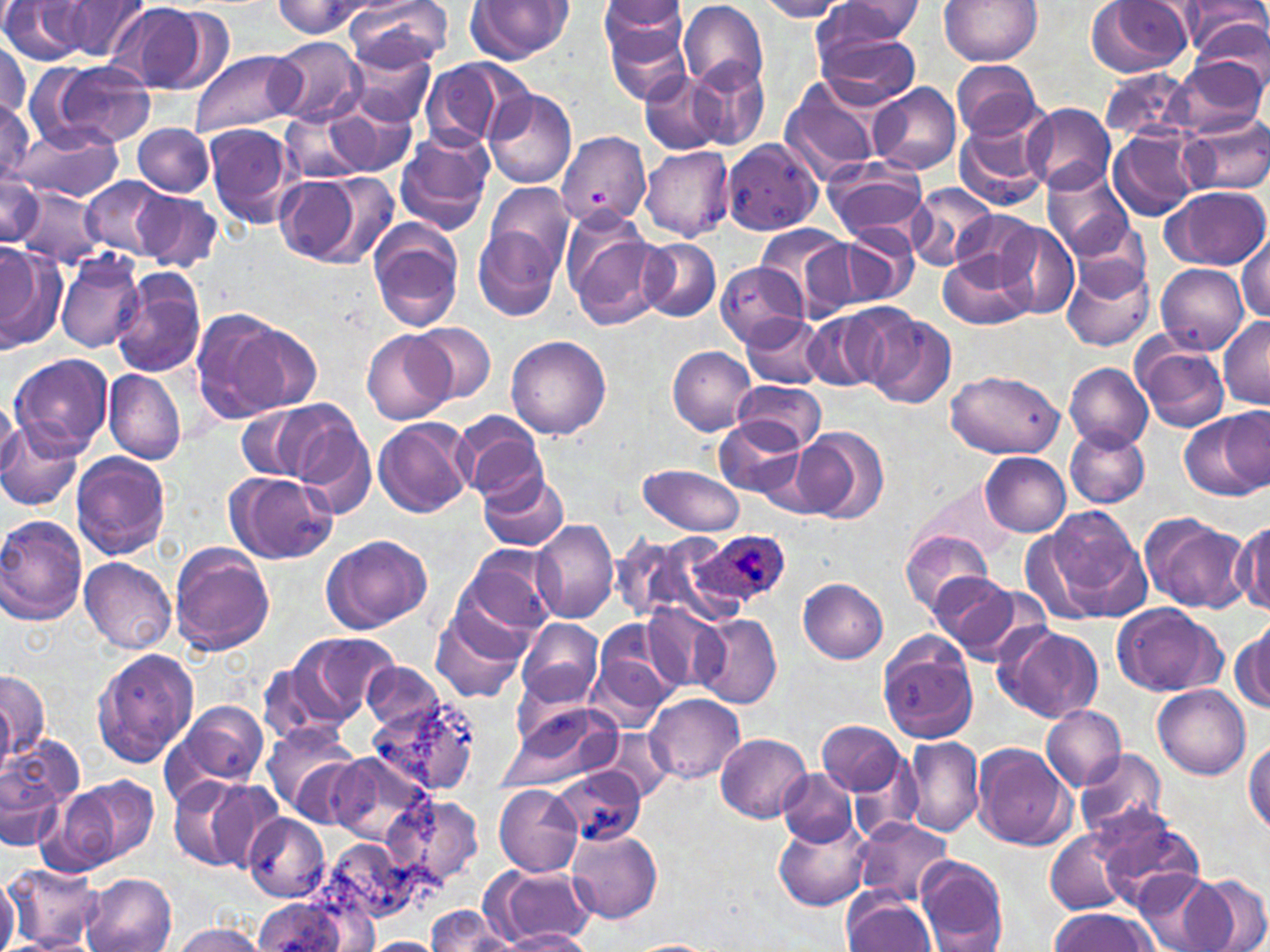

slide_level_diagnosis: Plasmodium ovale
uninfected_red_blood_cell_locations: 'approximate bounding boxes as named x1/y1/x2/y2 corners in pixels: (x1=1, y1=0, x2=90, y2=63), (x1=60, y1=0, x2=151, y2=62), (x1=275, y1=0, x2=376, y2=36), (x1=345, y1=0, x2=451, y2=73), (x1=464, y1=0, x2=573, y2=65), (x1=597, y1=0, x2=691, y2=86), (x1=756, y1=0, x2=848, y2=21), (x1=939, y1=0, x2=1042, y2=66), (x1=1085, y1=0, x2=1194, y2=78), (x1=1177, y1=0, x2=1268, y2=58), (x1=817, y1=1, x2=924, y2=53), (x1=679, y1=2, x2=768, y2=95), (x1=105, y1=3, x2=216, y2=95), (x1=126, y1=12, x2=264, y2=116), (x1=1190, y1=17, x2=1269, y2=88), (x1=814, y1=29, x2=922, y2=110), (x1=268, y1=37, x2=366, y2=126), (x1=0, y1=40, x2=30, y2=121), (x1=346, y1=46, x2=437, y2=128), (x1=189, y1=50, x2=301, y2=138), (x1=1171, y1=55, x2=1267, y2=137), (x1=688, y1=57, x2=770, y2=150), (x1=31, y1=59, x2=158, y2=151), (x1=950, y1=59, x2=1040, y2=141), (x1=418, y1=60, x2=512, y2=150), (x1=639, y1=68, x2=729, y2=155), (x1=1103, y1=70, x2=1196, y2=143), (x1=780, y1=77, x2=888, y2=182), (x1=868, y1=81, x2=962, y2=174), (x1=483, y1=87, x2=576, y2=189), (x1=0, y1=95, x2=48, y2=185), (x1=325, y1=104, x2=415, y2=177), (x1=1024, y1=104, x2=1114, y2=195), (x1=284, y1=109, x2=372, y2=185), (x1=954, y1=114, x2=1053, y2=212), (x1=1182, y1=116, x2=1270, y2=195), (x1=203, y1=122, x2=304, y2=230), (x1=132, y1=124, x2=215, y2=196), (x1=13, y1=127, x2=124, y2=201), (x1=394, y1=129, x2=495, y2=234), (x1=556, y1=131, x2=650, y2=230), (x1=1110, y1=131, x2=1199, y2=221), (x1=720, y1=138, x2=826, y2=239), (x1=640, y1=144, x2=735, y2=240), (x1=823, y1=159, x2=929, y2=246), (x1=1044, y1=166, x2=1135, y2=258), (x1=305, y1=170, x2=401, y2=267), (x1=0, y1=173, x2=42, y2=245), (x1=270, y1=174, x2=364, y2=265), (x1=81, y1=176, x2=173, y2=260), (x1=485, y1=184, x2=574, y2=274), (x1=905, y1=184, x2=1000, y2=270), (x1=18, y1=186, x2=104, y2=269), (x1=1164, y1=186, x2=1268, y2=270), (x1=134, y1=189, x2=223, y2=273), (x1=948, y1=208, x2=1044, y2=291), (x1=565, y1=219, x2=668, y2=330), (x1=367, y1=220, x2=466, y2=332), (x1=994, y1=220, x2=1081, y2=318), (x1=753, y1=223, x2=853, y2=316), (x1=840, y1=223, x2=917, y2=305), (x1=473, y1=227, x2=563, y2=321), (x1=1238, y1=233, x2=1269, y2=322), (x1=637, y1=238, x2=722, y2=322), (x1=0, y1=240, x2=64, y2=354), (x1=939, y1=248, x2=1035, y2=330), (x1=55, y1=250, x2=145, y2=354), (x1=1061, y1=255, x2=1153, y2=353), (x1=718, y1=262, x2=805, y2=346), (x1=1155, y1=263, x2=1248, y2=354), (x1=111, y1=271, x2=207, y2=378), (x1=188, y1=306, x2=310, y2=426), (x1=802, y1=310, x2=896, y2=391), (x1=861, y1=310, x2=957, y2=409), (x1=741, y1=313, x2=831, y2=388), (x1=1218, y1=314, x2=1270, y2=406), (x1=408, y1=321, x2=496, y2=406), (x1=362, y1=330, x2=453, y2=424), (x1=505, y1=335, x2=613, y2=438), (x1=1132, y1=338, x2=1229, y2=433), (x1=667, y1=345, x2=757, y2=434), (x1=8, y1=353, x2=114, y2=457), (x1=1064, y1=362, x2=1153, y2=453), (x1=104, y1=368, x2=186, y2=465), (x1=945, y1=370, x2=1064, y2=458), (x1=733, y1=378, x2=826, y2=452), (x1=0, y1=397, x2=22, y2=477), (x1=282, y1=404, x2=376, y2=518), (x1=235, y1=406, x2=325, y2=483), (x1=453, y1=411, x2=547, y2=501), (x1=1178, y1=411, x2=1269, y2=500), (x1=373, y1=418, x2=472, y2=519), (x1=715, y1=418, x2=807, y2=500), (x1=0, y1=419, x2=86, y2=514), (x1=793, y1=427, x2=889, y2=524), (x1=1065, y1=428, x2=1148, y2=508), (x1=70, y1=452, x2=171, y2=560), (x1=981, y1=454, x2=1070, y2=537), (x1=638, y1=463, x2=746, y2=537), (x1=224, y1=471, x2=339, y2=564), (x1=479, y1=471, x2=570, y2=551), (x1=915, y1=477, x2=1018, y2=564), (x1=1036, y1=504, x2=1150, y2=620), (x1=1140, y1=513, x2=1250, y2=610), (x1=0, y1=515, x2=89, y2=625), (x1=531, y1=519, x2=619, y2=625), (x1=1232, y1=521, x2=1268, y2=613), (x1=900, y1=529, x2=996, y2=616), (x1=612, y1=530, x2=734, y2=629), (x1=320, y1=534, x2=433, y2=634), (x1=461, y1=542, x2=560, y2=637), (x1=168, y1=543, x2=275, y2=655), (x1=437, y1=547, x2=545, y2=691), (x1=79, y1=557, x2=178, y2=653), (x1=930, y1=569, x2=1028, y2=658), (x1=799, y1=579, x2=888, y2=663), (x1=1111, y1=602, x2=1226, y2=697), (x1=643, y1=603, x2=729, y2=693), (x1=431, y1=609, x2=530, y2=704), (x1=696, y1=613, x2=781, y2=708), (x1=517, y1=619, x2=604, y2=705), (x1=1233, y1=621, x2=1270, y2=714), (x1=996, y1=624, x2=1102, y2=725), (x1=589, y1=627, x2=681, y2=728), (x1=283, y1=630, x2=399, y2=729), (x1=877, y1=630, x2=980, y2=743), (x1=92, y1=647, x2=199, y2=768), (x1=363, y1=662, x2=445, y2=732), (x1=0, y1=669, x2=49, y2=767), (x1=1153, y1=684, x2=1250, y2=779), (x1=645, y1=694, x2=744, y2=785), (x1=370, y1=695, x2=481, y2=799), (x1=173, y1=699, x2=268, y2=791), (x1=499, y1=702, x2=623, y2=794), (x1=1041, y1=705, x2=1125, y2=790), (x1=260, y1=721, x2=361, y2=822), (x1=817, y1=721, x2=908, y2=797), (x1=0, y1=732, x2=85, y2=844), (x1=715, y1=732, x2=812, y2=823), (x1=901, y1=735, x2=984, y2=836), (x1=1246, y1=736, x2=1270, y2=834), (x1=971, y1=742, x2=1075, y2=850), (x1=1074, y1=748, x2=1167, y2=843), (x1=321, y1=752, x2=432, y2=848), (x1=553, y1=766, x2=645, y2=846), (x1=778, y1=768, x2=858, y2=846), (x1=57, y1=776, x2=159, y2=870), (x1=167, y1=777, x2=268, y2=874), (x1=493, y1=783, x2=584, y2=877), (x1=382, y1=793, x2=484, y2=892), (x1=242, y1=813, x2=329, y2=903), (x1=1092, y1=813, x2=1207, y2=909), (x1=774, y1=817, x2=871, y2=911), (x1=851, y1=818, x2=955, y2=907), (x1=565, y1=826, x2=661, y2=926), (x1=1047, y1=827, x2=1133, y2=914), (x1=314, y1=838, x2=418, y2=932), (x1=914, y1=856, x2=1009, y2=951), (x1=5, y1=863, x2=99, y2=948), (x1=490, y1=866, x2=594, y2=946), (x1=0, y1=870, x2=20, y2=952), (x1=1133, y1=870, x2=1226, y2=952), (x1=80, y1=873, x2=177, y2=952), (x1=1186, y1=875, x2=1270, y2=952), (x1=843, y1=894, x2=937, y2=951), (x1=249, y1=898, x2=355, y2=951), (x1=426, y1=906, x2=513, y2=951), (x1=1049, y1=908, x2=1157, y2=951), (x1=167, y1=924, x2=270, y2=951), (x1=501, y1=929, x2=593, y2=951), (x1=10, y1=935, x2=97, y2=951), (x1=364, y1=937, x2=445, y2=952), (x1=628, y1=940, x2=714, y2=951)'
field_of_view: one of a larger specimen
preparation: thin blood film
plasmodium_ovale_infected_red_blood_cell_locations: 'approximate bounding boxes as named x1/y1/x2/y2 corners in pixels: (x1=694, y1=530, x2=789, y2=608)'
image_size: 1270×952 pixels
magnification: 1000x
stain: May-Grünwald-Giemsa
modality: optical microscopy